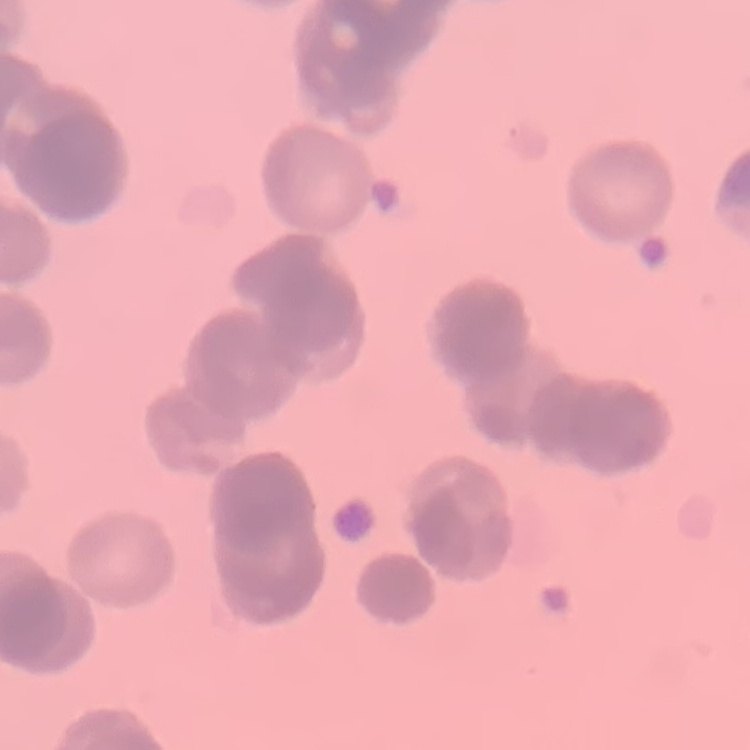

red blood cell morphology = rouleaux formation
image type = square crop of a larger photomicrograph
stain = Field's or Giemsa
preparation = thin blood smear